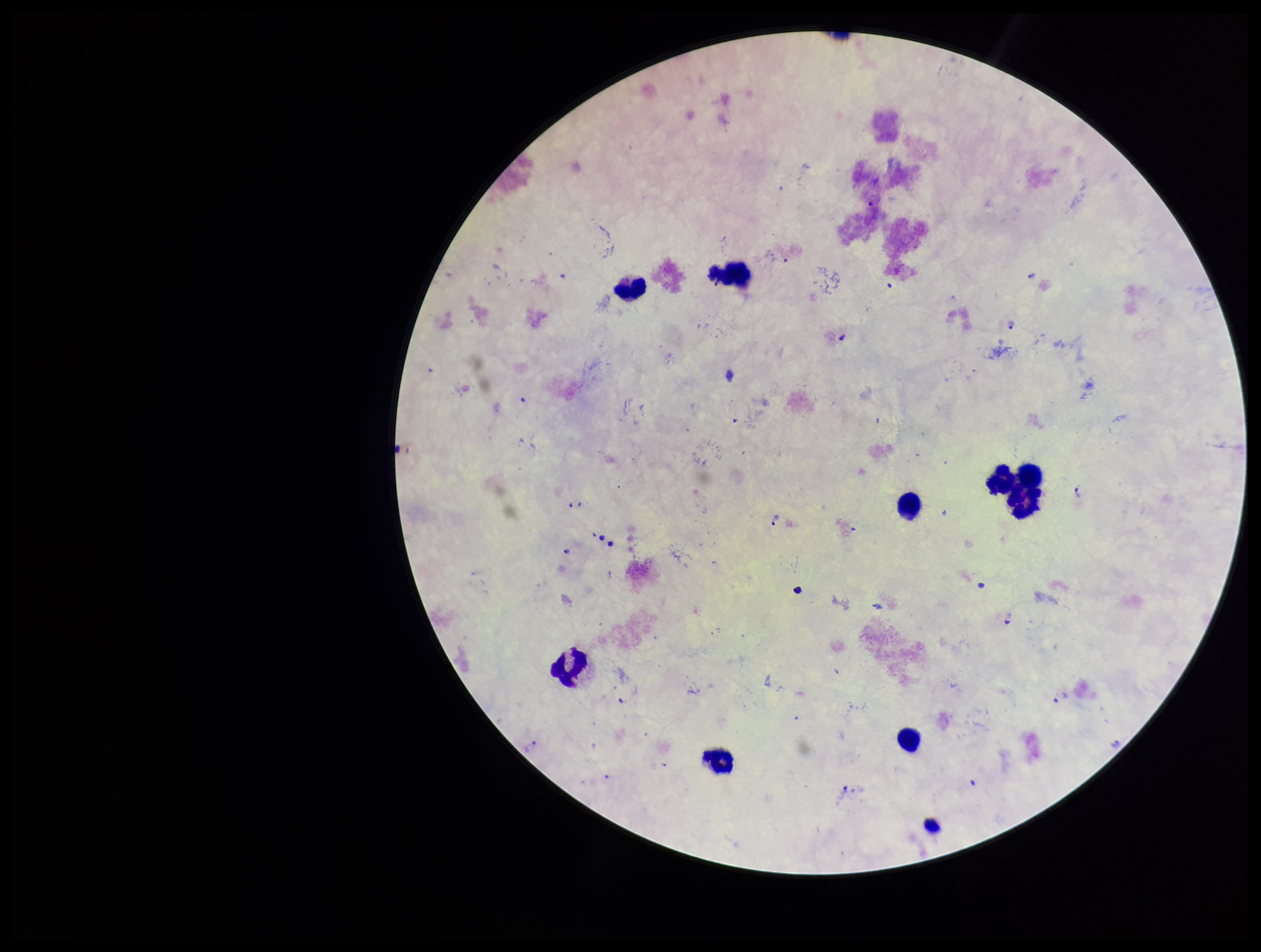
Plasmodium parasites: detected. Patient malaria status: positive. Stained with Giemsa. One field from this slide. Preparation: thick smear. Smartphone photograph taken through the eyepiece of a microscope. Parasite count: 3. Leukocyte count: 9. Image is 1261×952 pixels. Species reported for this patient: Plasmodium falciparum.